Report the malaria status of this cell.
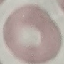
It is uninfected.

capture = smartphone camera at the microscope eyepiece
preparation = thin blood smear
image type = automatically extracted cell patch, resized to 64 × 64 pixels
stain = Giemsa